Describe the morphology of the red blood cells.
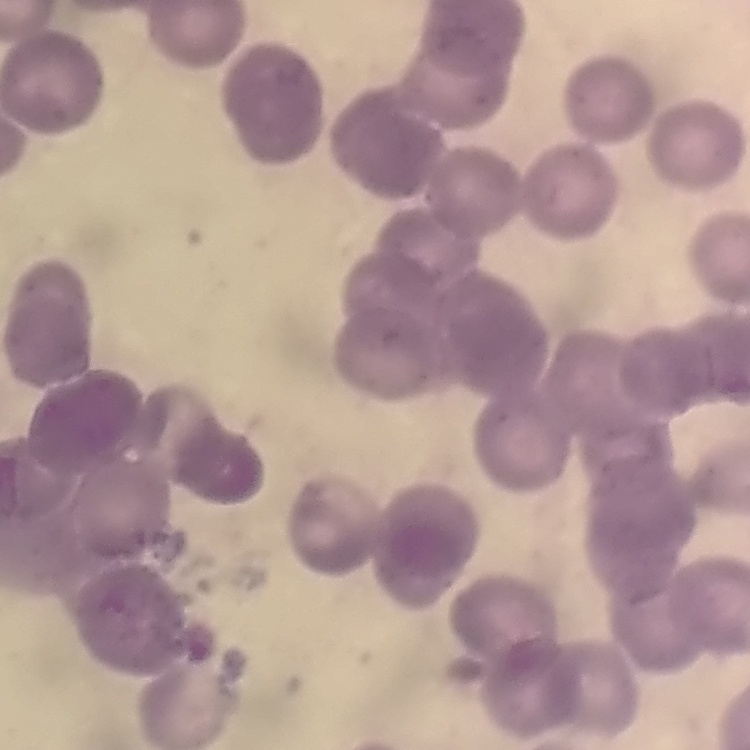
Rouleaux formation.

Summary:
  - Image type: square crop of a larger photomicrograph
  - Stain: Field's or Giemsa
  - Preparation: thin peripheral smear